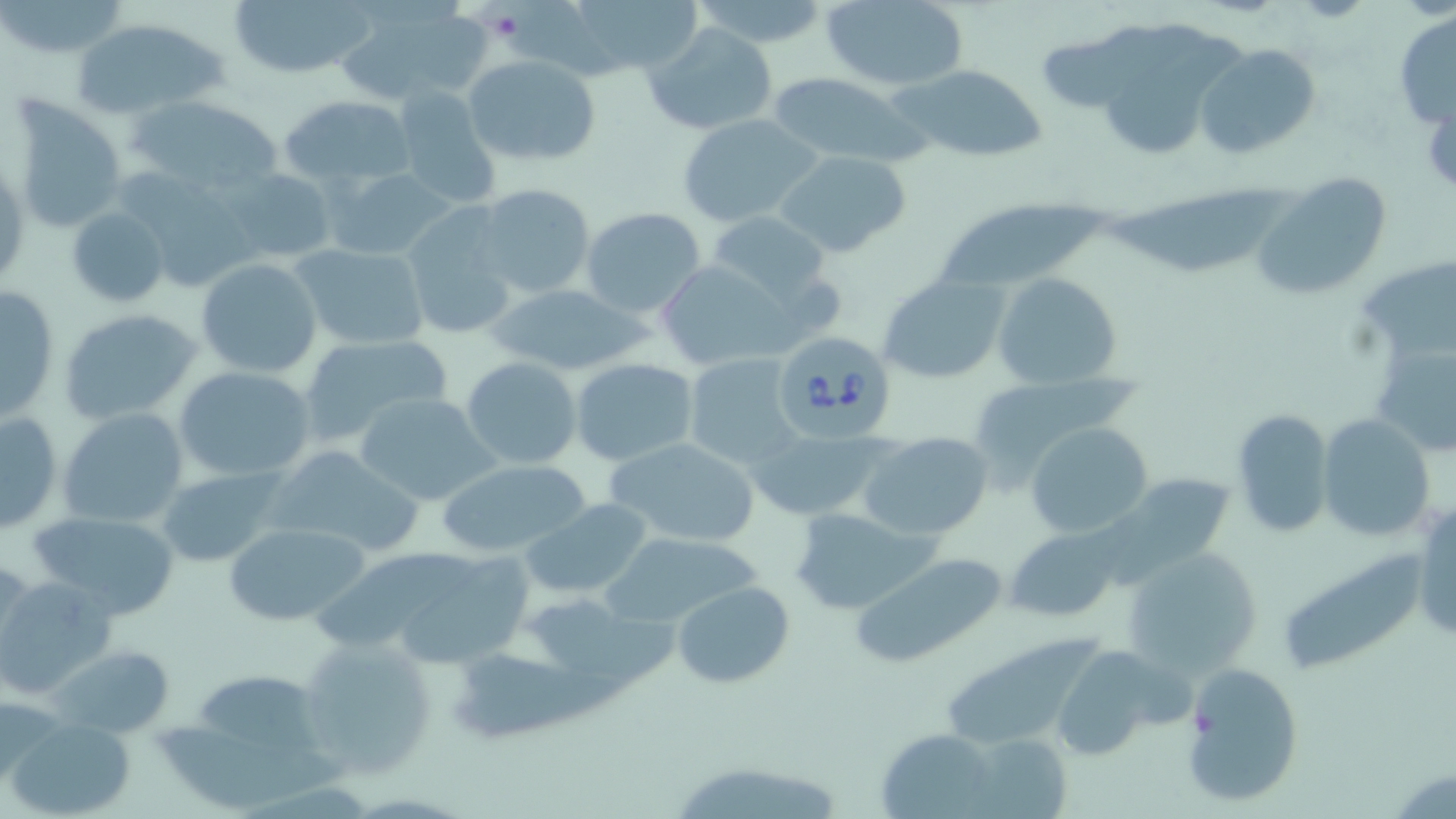
Approximate bounding boxes as [x1, y1, x2, y2] in pixels. Platelet locations: [484, 5, 527, 45]. Uninfected red blood cell locations: [227, 0, 376, 80], [572, 0, 701, 77], [690, 0, 828, 47], [819, 0, 969, 90], [0, 1, 131, 58], [506, 1, 626, 86], [335, 4, 484, 107], [1393, 8, 1456, 128], [70, 15, 228, 120], [1041, 18, 1202, 111], [643, 21, 780, 135], [1107, 33, 1244, 161], [1197, 43, 1321, 159], [465, 55, 601, 165], [895, 64, 1048, 162], [765, 71, 923, 166], [393, 87, 503, 210], [280, 92, 417, 191], [134, 93, 284, 194], [9, 96, 128, 234], [678, 113, 823, 227], [773, 149, 914, 259], [223, 166, 338, 264], [327, 168, 456, 261], [126, 172, 264, 299], [1253, 173, 1394, 303], [475, 182, 595, 298], [1105, 185, 1297, 279], [941, 188, 1112, 293], [399, 202, 521, 341], [65, 206, 171, 307], [580, 207, 707, 319], [704, 211, 834, 307], [291, 242, 432, 351], [1362, 256, 1456, 360], [196, 257, 323, 379], [654, 259, 790, 370], [992, 271, 1123, 390], [878, 274, 1009, 384], [1, 282, 60, 424], [489, 285, 644, 376], [58, 308, 203, 426], [297, 334, 452, 448], [1371, 338, 1455, 457], [682, 354, 803, 468], [462, 356, 582, 468], [569, 358, 699, 465], [173, 366, 314, 483], [964, 377, 1135, 481], [354, 392, 498, 506], [59, 408, 189, 529], [1232, 408, 1335, 535], [1, 409, 64, 533], [1317, 413, 1435, 543], [1025, 422, 1152, 538], [751, 428, 886, 520], [860, 431, 994, 540], [606, 437, 761, 549], [267, 443, 426, 559], [436, 457, 591, 557], [1084, 463, 1233, 590], [155, 468, 294, 567], [520, 497, 655, 601], [1413, 497, 1455, 642], [28, 508, 181, 619], [790, 509, 931, 613], [224, 520, 370, 627], [1006, 529, 1124, 622], [599, 531, 761, 629], [1122, 547, 1262, 677], [313, 548, 486, 648], [1277, 549, 1427, 680], [846, 550, 1009, 668], [404, 559, 538, 670], [0, 573, 117, 697], [671, 580, 795, 689], [530, 599, 675, 685], [294, 634, 439, 779], [941, 637, 1097, 750], [51, 644, 175, 737], [1047, 646, 1170, 760], [459, 652, 630, 741], [1181, 662, 1303, 807], [201, 669, 330, 759], [8, 714, 138, 819], [165, 715, 352, 813], [878, 730, 1001, 818], [979, 741, 1077, 816], [666, 759, 847, 819]. Babesia divergens-infected red blood cell locations: [768, 331, 900, 446]. Slide-level diagnosis: Babesia divergens. One field of a larger specimen. Image is 1456×819 pixels. Optical microscopy. May-Grünwald-Giemsa stain. 1000x magnification. Thin blood film.